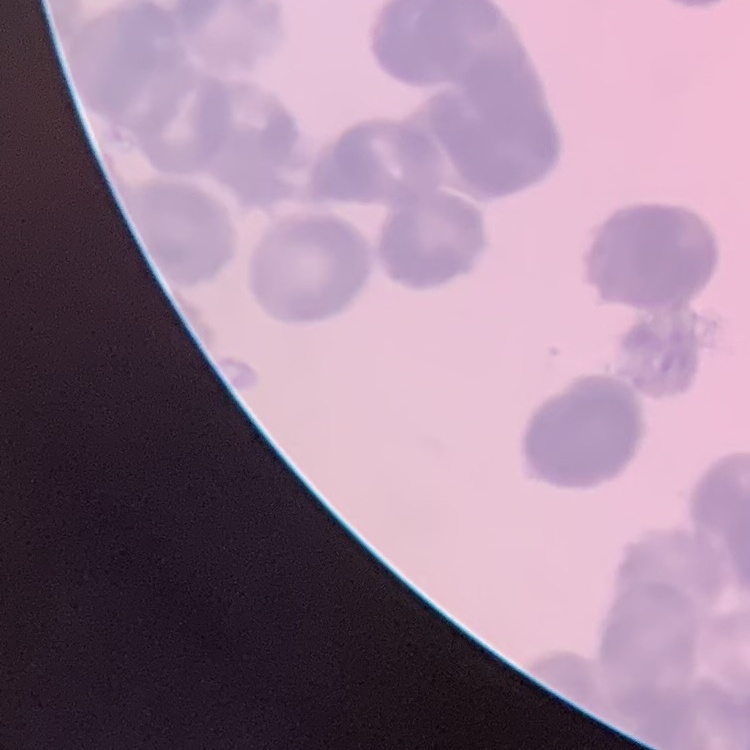

{
  "erythrocyte_morphology": "rouleaux formation",
  "preparation": "thin blood smear",
  "stain": "Field's or Giemsa",
  "image_type": "one tile cut from a larger photomicrograph"
}